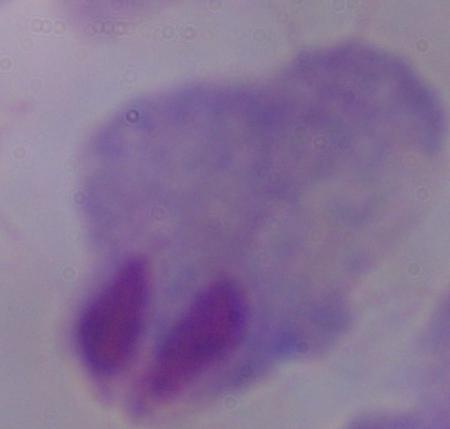

{
  "identification": "trichomonad",
  "magnification": "1000x",
  "modality": "micrograph"
}